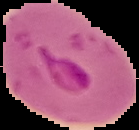

{
  "preparation": "thin blood film",
  "image_size": "139×130 pixels",
  "malaria_status": "parasitized",
  "image_type": "segmented cell region on a black background"
}